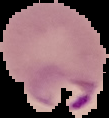

image_type: segmented cell region with the area outside set to black
image_size: 109×118 pixels
preparation: thin blood smear
result: malaria parasites identified